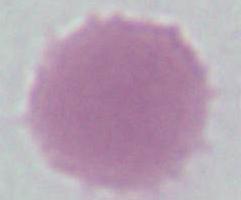
{
  "identification": "erythrocyte",
  "magnification": "1000x",
  "modality": "micrograph"
}